Evaluate for Plasmodium parasites.
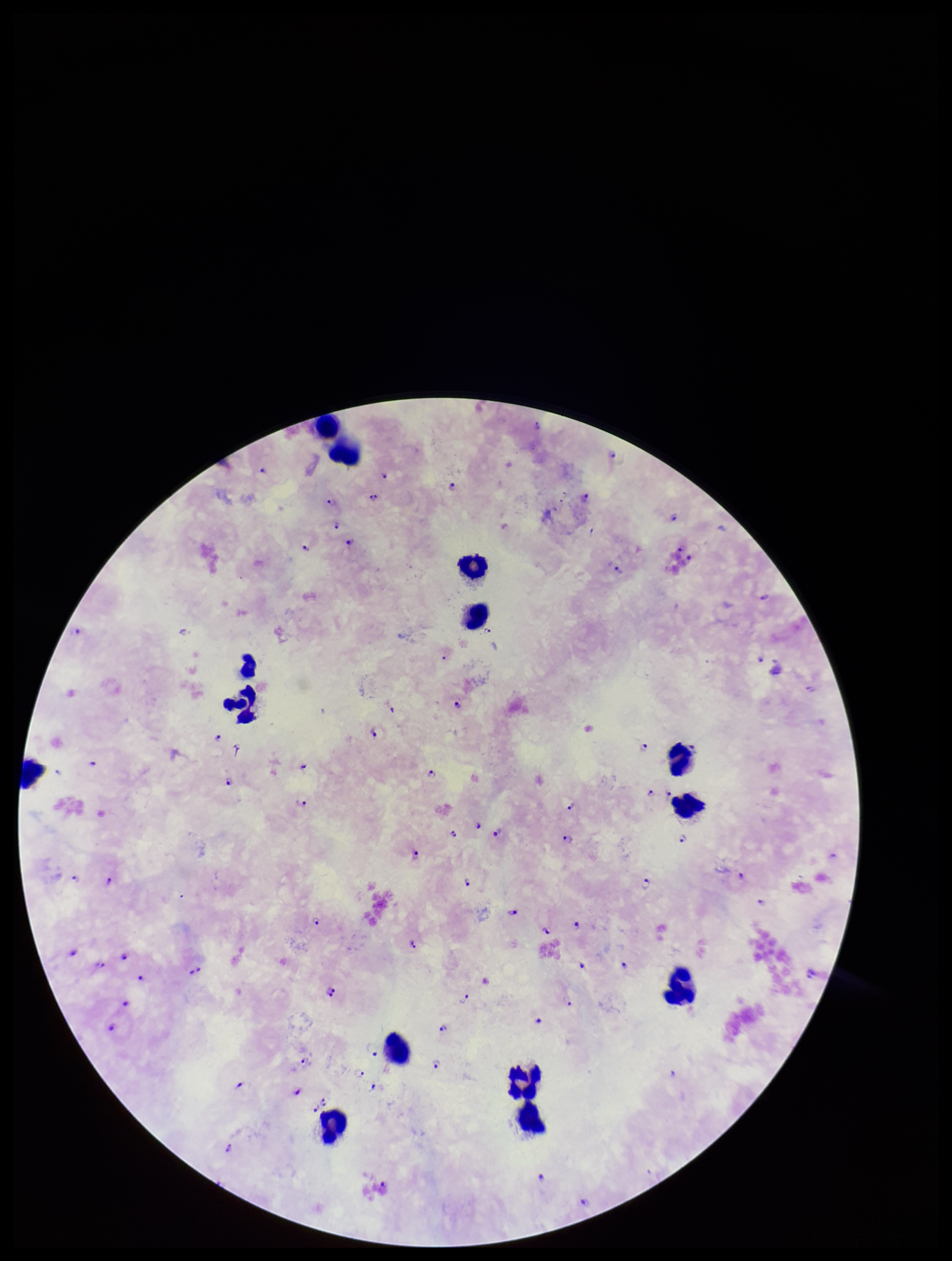
Detected.

Summary:
  - Stain: Giemsa
  - Patient malaria status: positive
  - Preparation: thick blood smear
  - Species reported for this patient: Plasmodium falciparum
  - Leukocyte count: 14
  - Field of view: single
  - Parasite count: 81
  - Capture: smartphone photograph through the microscope eyepiece
  - Image size: 952×1261 pixels